Describe the morphology of the erythrocytes.
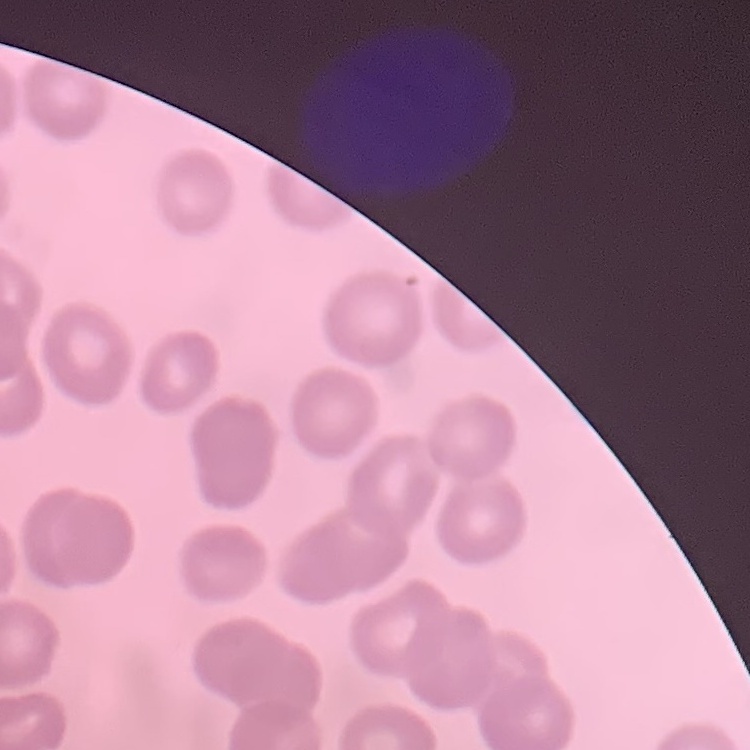
They show no rouleaux formation.

{
  "image_type": "square crop of a larger photomicrograph",
  "preparation": "thin blood smear",
  "stain": "Field's or Giemsa"
}